Locate every Plasmodium parasite.
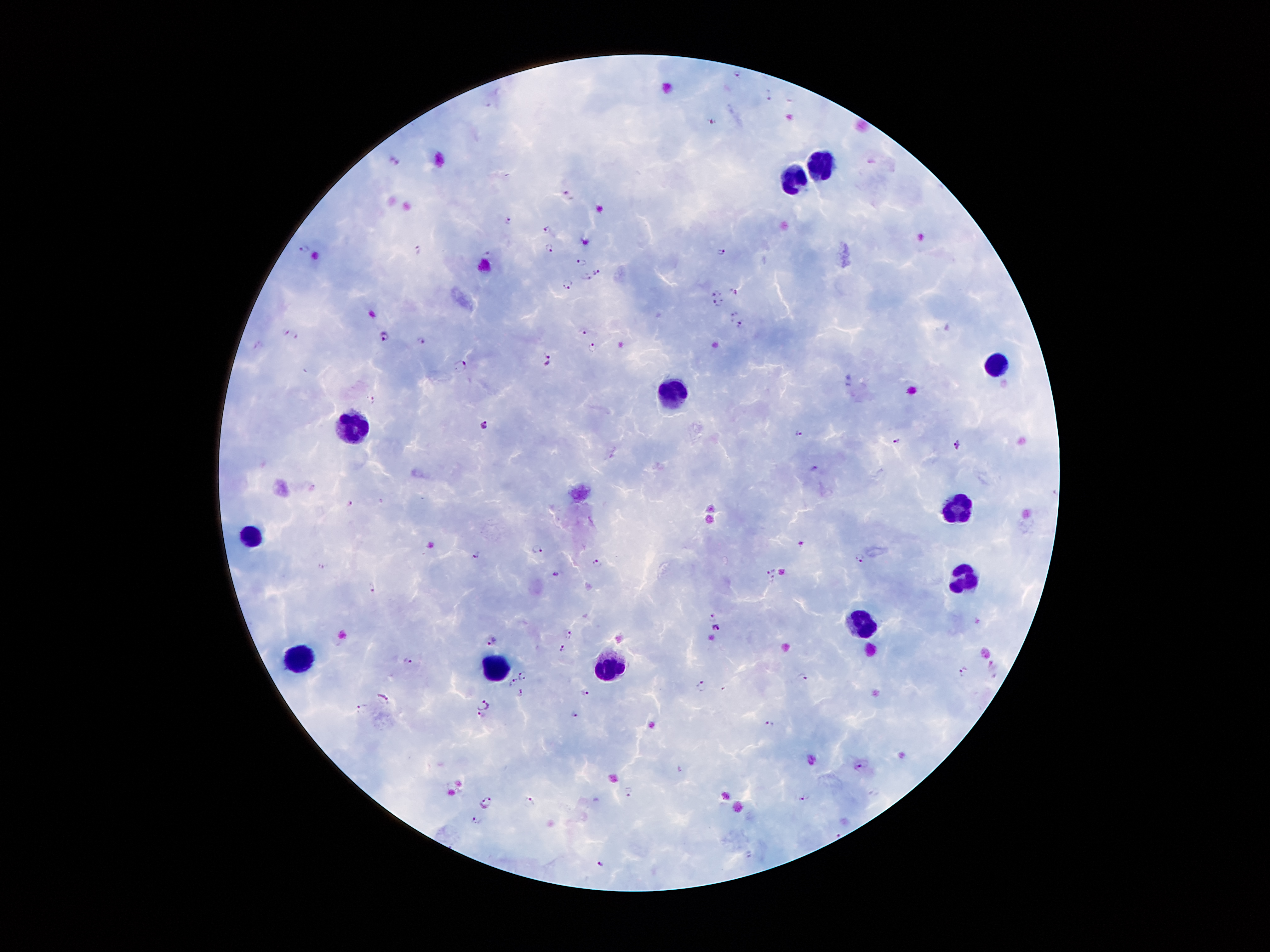
Approximate centers as [x, y] in pixels.
Plasmodium parasites: [736, 72], [768, 94], [490, 101], [710, 119], [395, 160], [569, 194], [507, 221], [547, 229], [307, 248], [418, 248], [548, 248], [722, 251], [489, 255], [582, 263], [598, 272], [586, 277], [568, 285], [734, 290], [717, 293], [717, 303], [734, 314], [740, 324], [584, 331], [286, 332], [297, 334], [383, 335], [422, 341], [594, 348], [546, 358], [462, 366], [372, 400], [483, 423], [798, 434], [898, 442], [957, 442], [814, 468], [351, 504], [801, 543], [539, 549], [476, 555], [861, 557], [596, 562], [771, 571], [556, 574], [371, 588], [712, 615], [715, 627], [568, 632], [494, 640], [561, 648], [408, 660], [964, 670], [522, 675], [803, 676], [515, 683], [702, 686], [521, 692], [585, 693], [381, 697], [483, 704], [362, 708], [482, 715], [575, 715], [771, 723], [859, 768], [631, 791], [806, 796], [529, 800], [487, 801], [476, 820], [837, 833], [600, 864].

preparation: thick peripheral-blood smear
stain: Giemsa
magnification: 100x
patient_malaria_status: positive for Plasmodium falciparum
image_size: 1270×952 pixels
leukocyte_locations: 'approximate centers as [x, y] in pixels: [828, 164], [794, 182], [996, 362], [676, 390], [353, 428], [964, 505], [253, 537], [962, 578], [858, 621], [296, 658], [497, 666], [615, 666]'
capture: smartphone camera through the microscope eyepiece
field_of_view: one from this slide